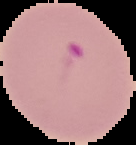
Summary:
  - Image size: 136×145 pixels
  - Preparation: thin blood smear
  - Image type: cell region segmented out of the field of view; surrounding area masked to black
  - Malaria status: parasitized